Report the malaria status of this cell.
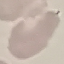

It is uninfected.

image_type: automatically extracted cell patch, resized to 64 × 64 pixels
stain: Giemsa
preparation: thin blood film
capture: smartphone camera at the microscope eyepiece